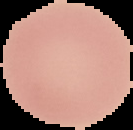
From a thin blood smear. The area outside the segmented cell region is set to black. Result: negative for malaria parasites. Image is 133×130 pixels.